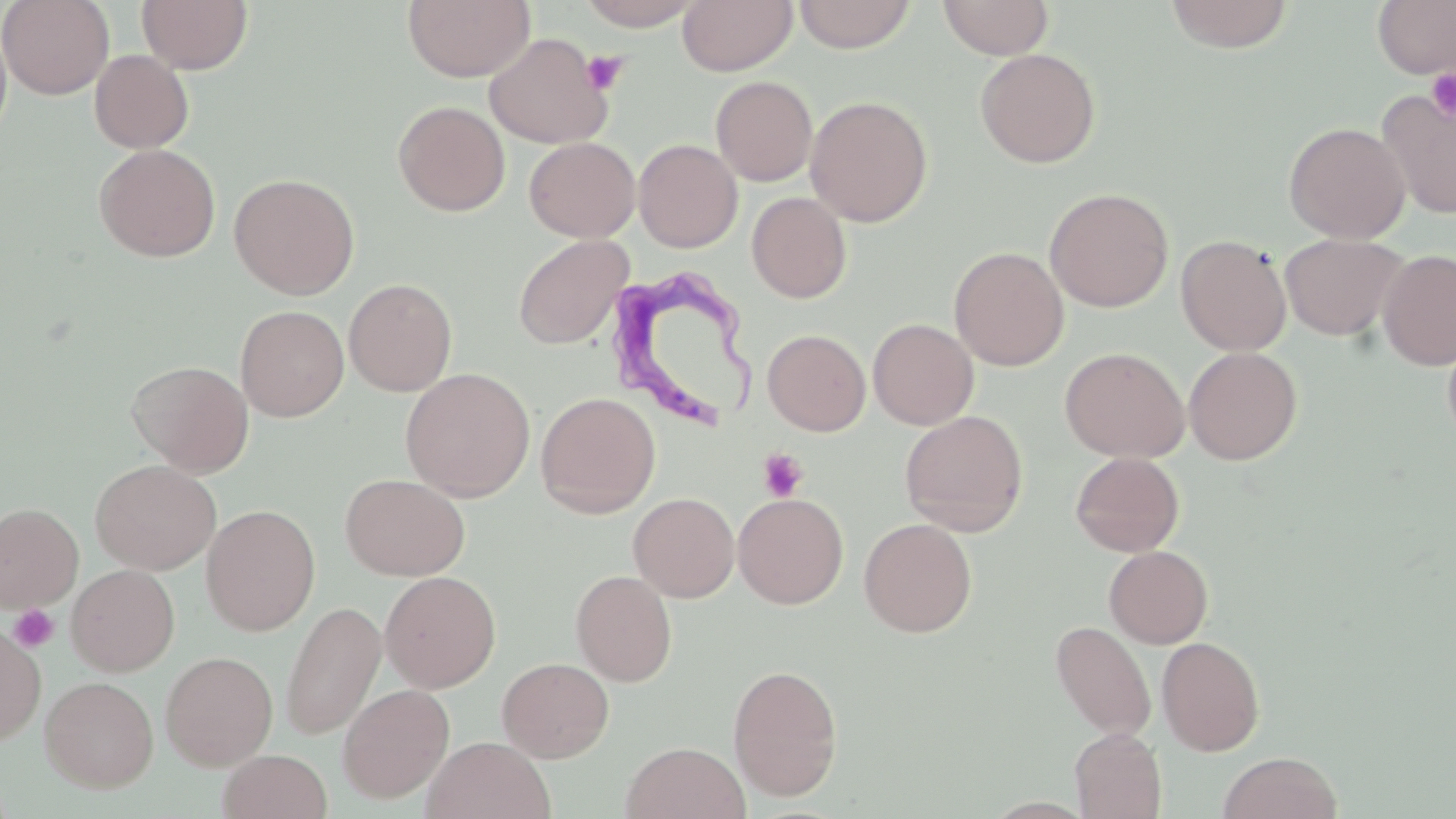
Summary:
  - Coordinate format: approximate bounding boxes as named x1/y1/x2/y2 corners in pixels
  - Platelet locations: (x1=582, y1=50, x2=628, y2=95), (x1=1426, y1=68, x2=1456, y2=120), (x1=758, y1=449, x2=808, y2=501), (x1=10, y1=605, x2=59, y2=652)
  - Trypanosoma brucei locations: (x1=611, y1=265, x2=763, y2=431)
  - Uninfected red blood cell locations: (x1=0, y1=0, x2=114, y2=99), (x1=136, y1=0, x2=253, y2=74), (x1=402, y1=0, x2=535, y2=83), (x1=576, y1=0, x2=704, y2=30), (x1=678, y1=0, x2=797, y2=76), (x1=793, y1=0, x2=917, y2=53), (x1=938, y1=0, x2=1053, y2=59), (x1=1163, y1=0, x2=1295, y2=53), (x1=1372, y1=1, x2=1456, y2=79), (x1=0, y1=17, x2=13, y2=149), (x1=483, y1=32, x2=614, y2=149), (x1=975, y1=48, x2=1100, y2=169), (x1=89, y1=50, x2=194, y2=153), (x1=710, y1=76, x2=818, y2=186), (x1=1376, y1=88, x2=1456, y2=220), (x1=805, y1=95, x2=933, y2=226), (x1=392, y1=100, x2=510, y2=216), (x1=1283, y1=121, x2=1411, y2=244), (x1=524, y1=136, x2=640, y2=242), (x1=633, y1=139, x2=742, y2=252), (x1=94, y1=143, x2=220, y2=262), (x1=228, y1=173, x2=360, y2=300), (x1=1044, y1=187, x2=1174, y2=312), (x1=746, y1=192, x2=852, y2=303), (x1=1279, y1=233, x2=1410, y2=341), (x1=513, y1=235, x2=634, y2=350), (x1=1175, y1=235, x2=1292, y2=355), (x1=949, y1=246, x2=1069, y2=371), (x1=1377, y1=248, x2=1456, y2=371), (x1=344, y1=278, x2=457, y2=395), (x1=235, y1=305, x2=349, y2=422), (x1=868, y1=318, x2=979, y2=429), (x1=1442, y1=327, x2=1456, y2=450), (x1=763, y1=329, x2=871, y2=436), (x1=1183, y1=346, x2=1302, y2=465), (x1=1059, y1=347, x2=1191, y2=463), (x1=127, y1=360, x2=254, y2=477), (x1=400, y1=367, x2=536, y2=501), (x1=536, y1=391, x2=660, y2=518), (x1=899, y1=410, x2=1029, y2=536), (x1=1070, y1=452, x2=1185, y2=557), (x1=90, y1=459, x2=221, y2=575), (x1=339, y1=472, x2=470, y2=581), (x1=628, y1=492, x2=740, y2=602), (x1=733, y1=492, x2=848, y2=609), (x1=0, y1=503, x2=83, y2=612), (x1=201, y1=504, x2=321, y2=636), (x1=859, y1=517, x2=977, y2=638), (x1=1104, y1=545, x2=1213, y2=648), (x1=66, y1=564, x2=180, y2=676), (x1=571, y1=569, x2=677, y2=686), (x1=380, y1=570, x2=501, y2=693), (x1=280, y1=600, x2=386, y2=740), (x1=1050, y1=620, x2=1156, y2=741), (x1=0, y1=624, x2=46, y2=743), (x1=1157, y1=636, x2=1265, y2=756), (x1=161, y1=651, x2=278, y2=770), (x1=497, y1=657, x2=614, y2=763), (x1=727, y1=664, x2=843, y2=801), (x1=40, y1=676, x2=158, y2=792), (x1=338, y1=682, x2=455, y2=803), (x1=1070, y1=728, x2=1166, y2=819), (x1=422, y1=736, x2=555, y2=819), (x1=622, y1=741, x2=749, y2=819), (x1=218, y1=749, x2=332, y2=819), (x1=1217, y1=751, x2=1342, y2=819)
  - Slide-level diagnosis: Trypanosoma brucei
  - Preparation: thin blood film
  - Stain: May-Grünwald-Giemsa
  - Modality: optical microscopy
  - Image size: 1456×819 pixels
  - Magnification: 1000x
  - Field of view: one of a larger specimen